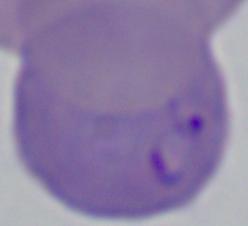
{
  "magnification": "1000x",
  "modality": "micrograph",
  "identification": "Babesia"
}